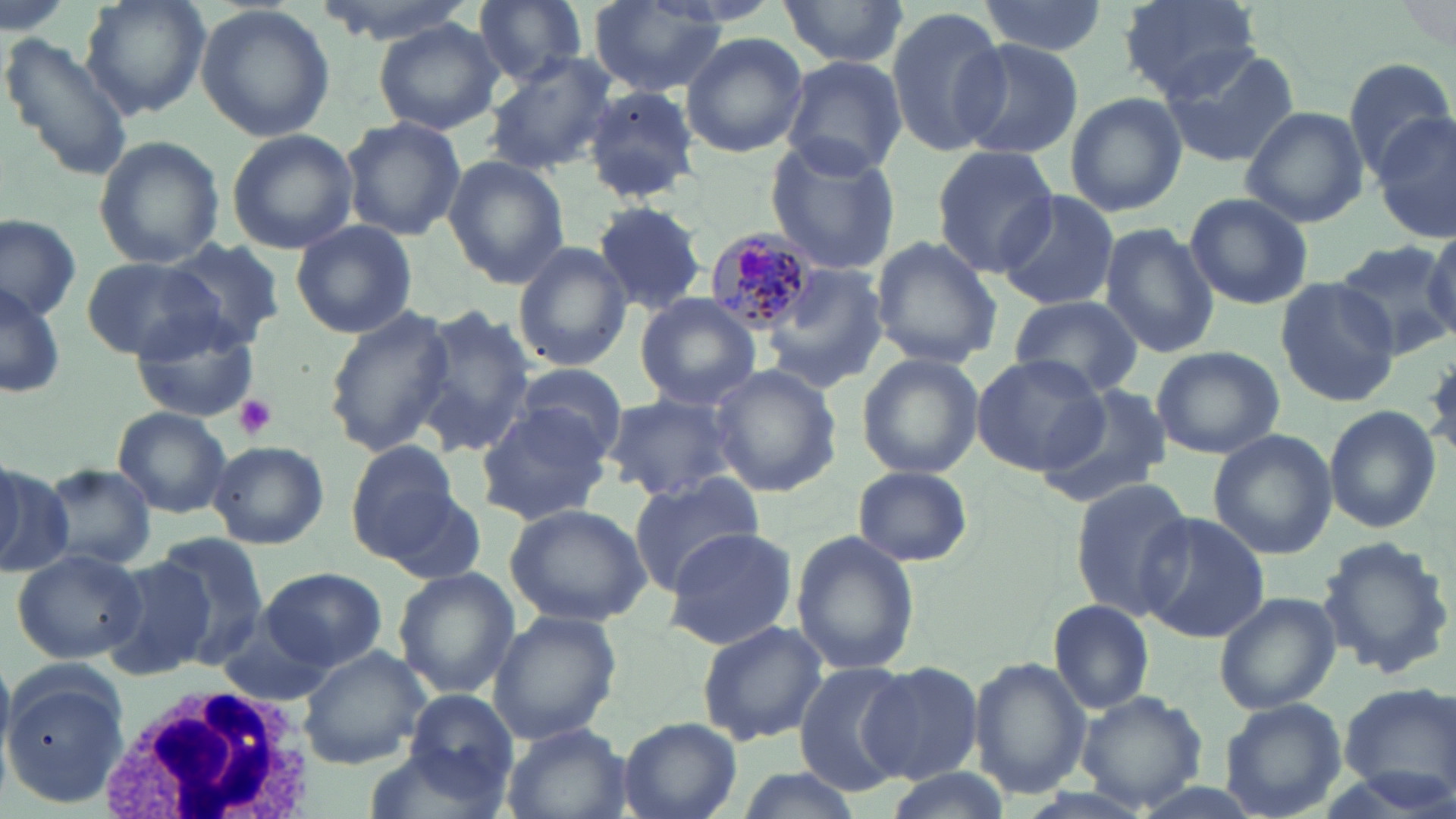
Summary:
  - Coordinate format: approximate bounding boxes as [x1, y1, x2, y2] in pixels
  - White blood cell locations: [99, 676, 319, 819]
  - Platelet locations: [234, 395, 278, 440]
  - Plasmodium malariae-infected red blood cell locations: [704, 227, 818, 336]
  - Uninfected red blood cell locations: [78, 0, 211, 119], [309, 0, 479, 43], [778, 0, 910, 71], [977, 0, 1109, 57], [1119, 0, 1261, 99], [472, 1, 591, 84], [589, 3, 729, 96], [194, 4, 335, 143], [886, 5, 1014, 158], [373, 18, 505, 136], [0, 31, 134, 181], [680, 31, 809, 159], [951, 37, 1085, 160], [1158, 43, 1301, 168], [483, 51, 619, 174], [779, 57, 908, 180], [1343, 57, 1454, 178], [581, 87, 701, 203], [1061, 92, 1187, 216], [1240, 106, 1369, 226], [1372, 113, 1456, 242], [340, 116, 467, 243], [225, 129, 358, 253], [91, 134, 225, 270], [764, 140, 902, 274], [932, 146, 1060, 277], [441, 155, 570, 288], [996, 190, 1123, 314], [1182, 193, 1313, 310], [589, 202, 706, 316], [0, 215, 80, 322], [290, 219, 418, 339], [1097, 223, 1218, 357], [1420, 227, 1456, 345], [870, 234, 1003, 368], [162, 238, 287, 350], [1331, 239, 1456, 360], [512, 242, 632, 372], [81, 258, 227, 360], [768, 261, 888, 394], [1, 276, 66, 405], [1276, 278, 1400, 405], [633, 293, 763, 411], [1008, 296, 1143, 399], [323, 306, 456, 458], [408, 306, 537, 454], [130, 311, 261, 423], [1152, 345, 1283, 461], [857, 353, 984, 480], [970, 354, 1107, 475], [508, 363, 627, 464], [710, 365, 842, 499], [1036, 385, 1170, 509], [602, 393, 741, 502], [475, 400, 612, 524], [1324, 406, 1441, 533], [112, 407, 233, 517], [1208, 428, 1337, 558], [208, 439, 329, 548], [347, 440, 463, 558], [37, 462, 159, 572], [0, 464, 62, 571], [852, 465, 974, 566], [626, 472, 762, 594], [1069, 478, 1199, 620], [380, 486, 489, 588], [504, 501, 653, 626], [1138, 513, 1273, 643], [662, 528, 799, 648], [789, 530, 920, 678], [1314, 534, 1454, 681], [151, 536, 267, 661], [12, 546, 149, 663], [99, 556, 215, 680], [261, 566, 388, 671], [393, 569, 519, 698], [1214, 591, 1341, 716], [1049, 599, 1155, 713], [487, 610, 621, 744], [694, 619, 829, 745], [213, 622, 338, 708], [296, 647, 433, 768], [969, 656, 1090, 800], [860, 661, 983, 785], [794, 663, 916, 796], [3, 671, 127, 804], [1335, 683, 1456, 802], [1075, 688, 1208, 812], [406, 691, 517, 796], [1219, 699, 1347, 819], [619, 717, 741, 819], [501, 723, 633, 819], [361, 742, 512, 818]
  - Slide-level diagnosis: Plasmodium malariae
  - Field of view: one of a larger specimen
  - Magnification: 1000x
  - Image size: 1456×819 pixels
  - Stain: May-Grünwald-Giemsa
  - Preparation: thin blood film
  - Modality: light microscopy